Classify this cell by malaria status.
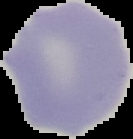

Uninfected.

Cell region segmented out of the field of view; the surrounding area is masked to black. Image is 133×139 pixels. From a thin blood smear.